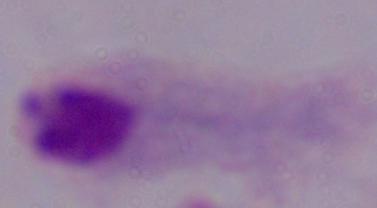 Photomicrograph. A trichomonad is seen. Captured at 1000x magnification.